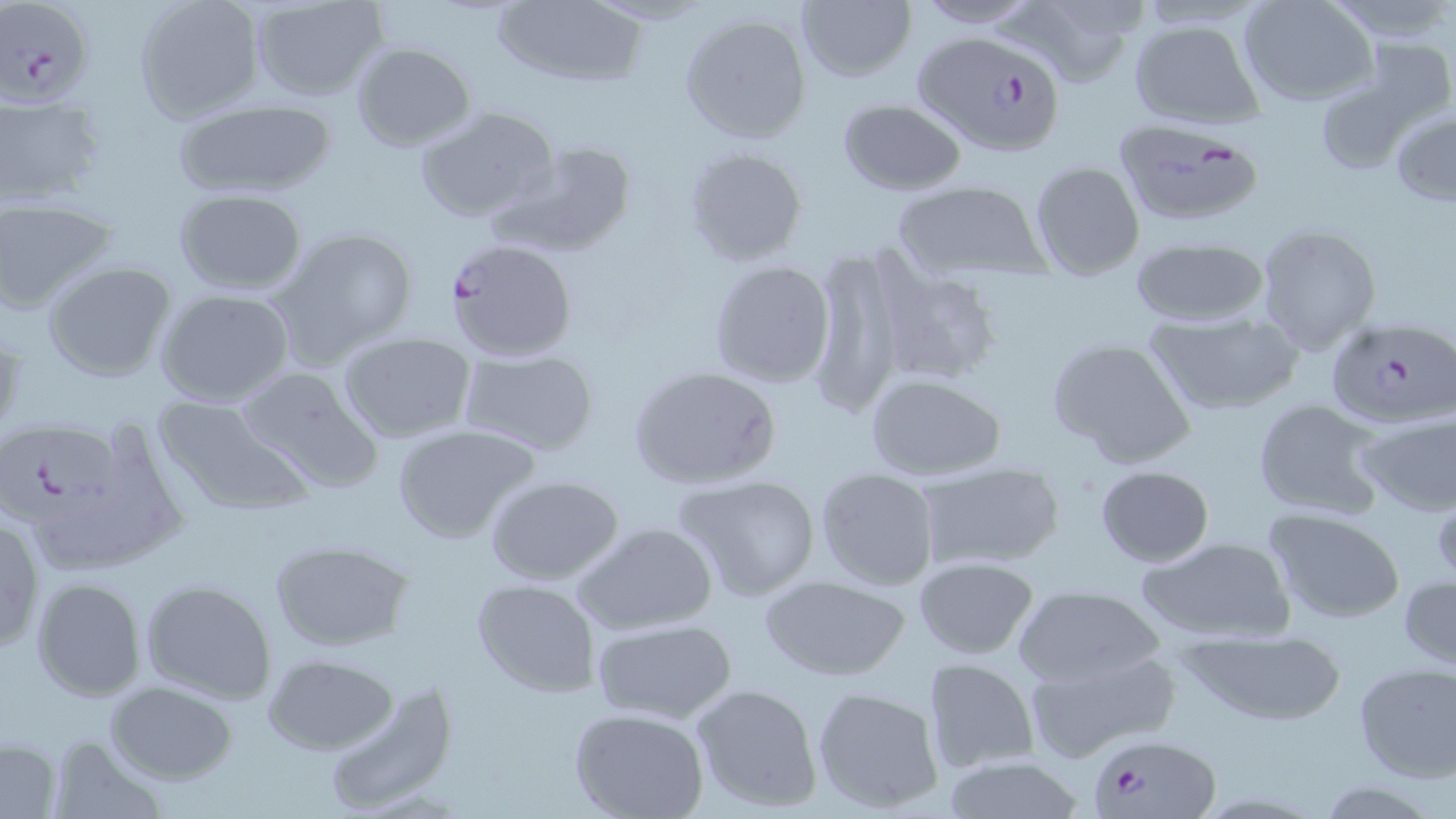
Approximate bounding boxes as [x1, y1, x2, y2] in pixels. Uninfected red blood cell locations: [133, 0, 265, 124], [910, 0, 1043, 28], [1329, 0, 1453, 44], [248, 1, 386, 101], [490, 1, 647, 86], [794, 1, 917, 84], [1002, 1, 1149, 87], [1238, 1, 1379, 106], [678, 12, 813, 145], [1125, 17, 1267, 130], [1351, 38, 1454, 136], [351, 43, 477, 150], [1315, 80, 1422, 175], [0, 92, 107, 207], [171, 98, 338, 198], [838, 98, 967, 196], [416, 105, 560, 224], [1389, 106, 1456, 205], [493, 139, 638, 256], [684, 145, 808, 267], [1029, 160, 1145, 279], [888, 179, 1054, 282], [173, 188, 307, 295], [0, 198, 118, 314], [1255, 223, 1383, 356], [269, 224, 419, 367], [1129, 234, 1270, 328], [808, 249, 905, 419], [707, 260, 836, 389], [42, 261, 178, 382], [870, 261, 1002, 388], [154, 288, 297, 408], [1144, 311, 1304, 415], [1, 326, 25, 437], [337, 331, 479, 442], [1046, 336, 1197, 469], [457, 350, 599, 456], [627, 364, 783, 490], [236, 365, 385, 494], [864, 373, 1006, 482], [150, 396, 309, 517], [1251, 397, 1388, 520], [1353, 410, 1455, 516], [390, 423, 543, 545], [913, 461, 1065, 572], [1095, 465, 1214, 566], [814, 467, 940, 592], [671, 473, 822, 602], [484, 475, 626, 586], [1264, 508, 1406, 623], [0, 513, 44, 654], [574, 521, 718, 636], [1136, 535, 1298, 644], [268, 539, 416, 652], [912, 556, 1039, 659], [1399, 572, 1456, 671], [760, 574, 909, 681], [30, 577, 147, 701], [139, 577, 277, 703], [471, 577, 601, 698], [1010, 584, 1168, 689], [590, 618, 737, 726], [1173, 629, 1349, 723], [1024, 648, 1180, 762], [264, 654, 399, 755], [922, 657, 1040, 774], [1352, 663, 1455, 782], [320, 680, 462, 817], [104, 681, 238, 784], [689, 682, 823, 811], [811, 684, 948, 815], [570, 709, 711, 819], [47, 735, 168, 818], [1, 737, 64, 816], [940, 756, 1089, 817]. Plasmodium falciparum-infected red blood cell locations: [2, 0, 91, 104], [913, 28, 1066, 161], [1112, 118, 1266, 230], [443, 237, 577, 361], [1328, 315, 1456, 426], [1, 417, 113, 532], [1093, 731, 1219, 818]. Slide-level diagnosis: Plasmodium falciparum. Optical microscopy. May-Grünwald-Giemsa-stained preparation. One field of a larger specimen. Image is 1456×819 pixels. 1000x magnification. Thin blood film.